Classify this cell by malaria status.
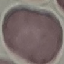

It is uninfected.

image type = cell patch, automatically extracted from a larger field of view and resized to 64 × 64 pixels
stain = Giemsa
preparation = thin blood film
capture = smartphone camera at the microscope eyepiece